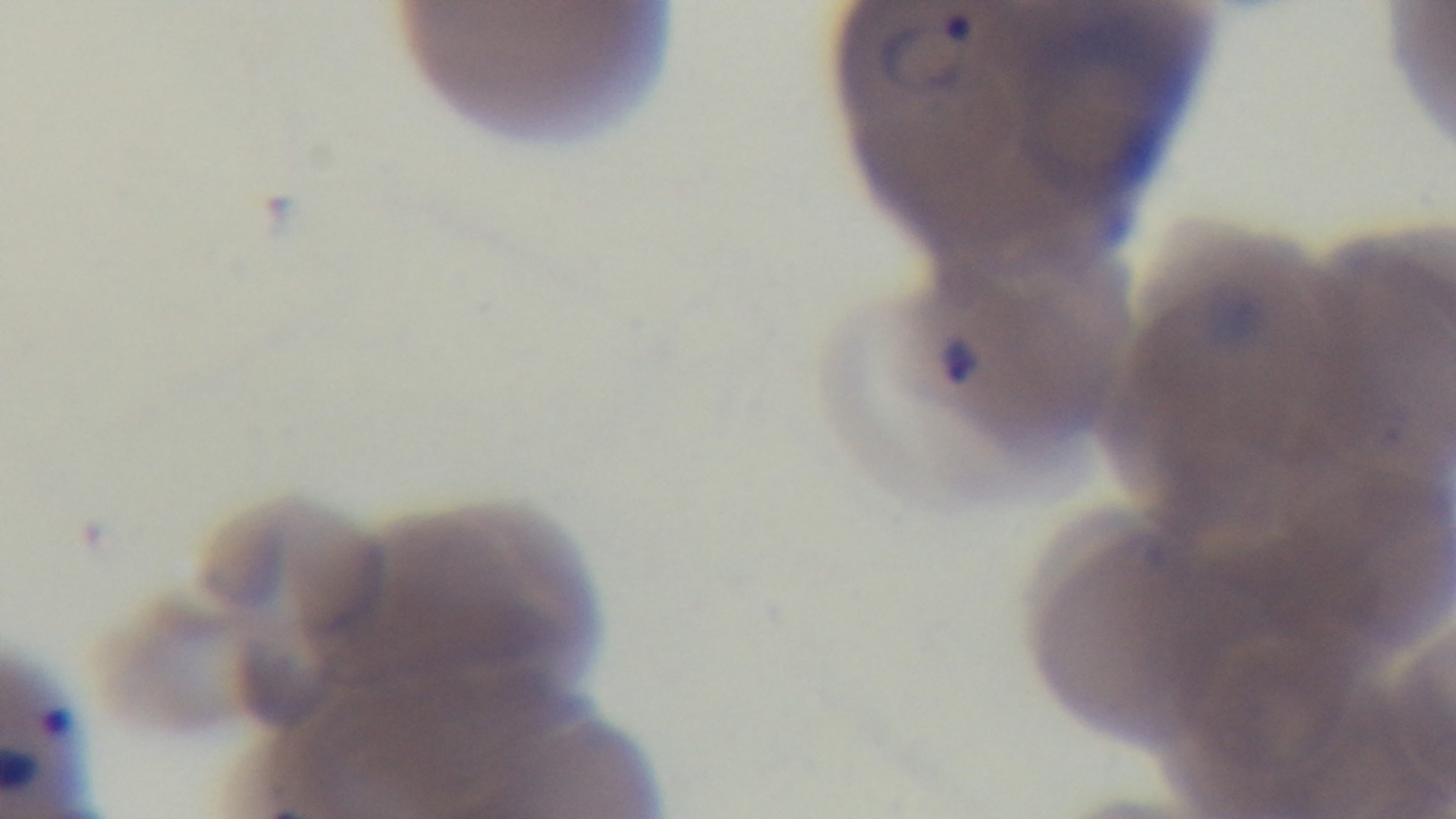 Oil-immersion objective, 100x. Mounted 4K digital camera. One field from the slide. Photomicrograph. Giemsa stain. Malaria status: positive. Preparation: thin.